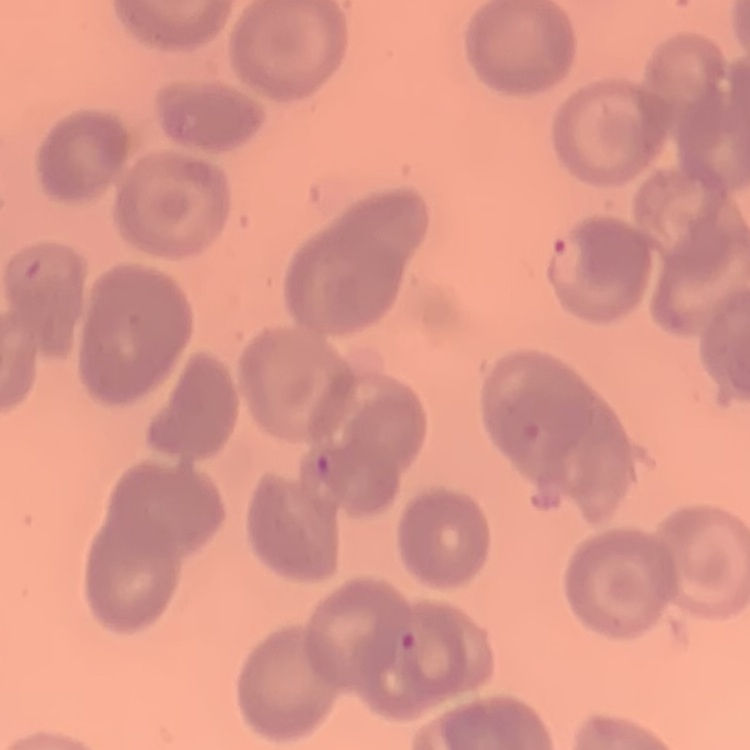
erythrocyte morphology = no rouleaux formation
image type = square crop of a larger photomicrograph
preparation = thin peripheral smear
stain = Field's or Giemsa